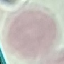

malaria status = uninfected
image type = cell patch, automatically extracted from a larger field of view and resized to 64 × 64 pixels
capture = smartphone camera at the microscope eyepiece
preparation = thin blood film
stain = Giemsa